Locate every Plasmodium falciparum-infected red blood cell.
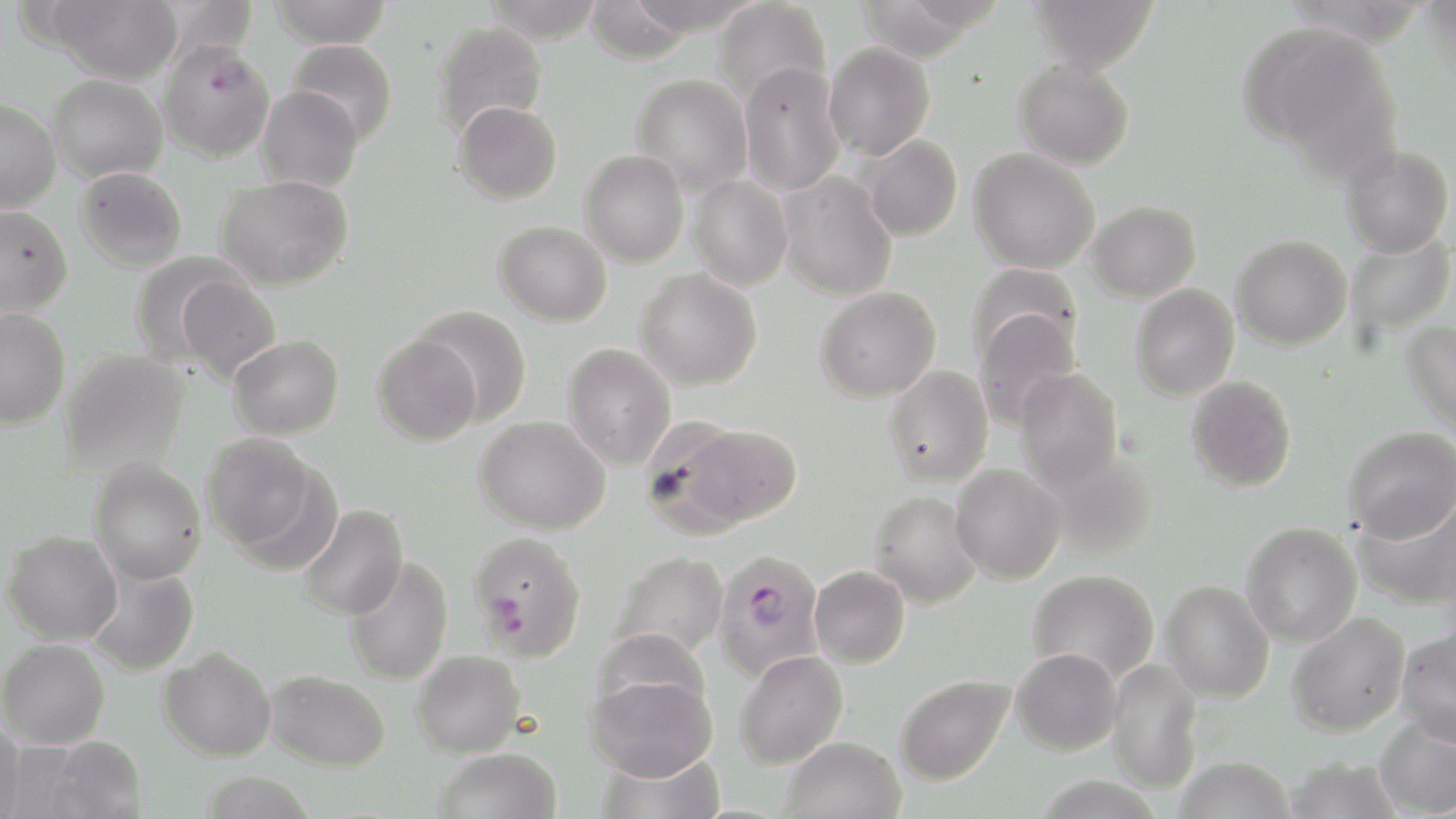
Approximate bounding boxes as [x1, y1, x2, y2] in pixels.
Plasmodium falciparum-infected red blood cells: [157, 39, 276, 162], [467, 530, 587, 661], [713, 550, 826, 681].

Uninfected red blood cell locations: [41, 0, 184, 84], [269, 0, 394, 49], [713, 0, 832, 109], [1027, 0, 1159, 72], [585, 1, 693, 64], [851, 1, 989, 62], [433, 20, 548, 137], [1238, 20, 1396, 162], [287, 39, 398, 146], [824, 41, 935, 160], [1014, 58, 1135, 169], [739, 62, 845, 197], [47, 73, 168, 183], [632, 73, 753, 197], [257, 85, 364, 193], [0, 98, 61, 212], [453, 100, 563, 204], [858, 134, 963, 242], [1340, 145, 1454, 258], [969, 148, 1100, 274], [579, 149, 689, 267], [75, 167, 187, 272], [777, 171, 898, 301], [216, 175, 353, 291], [688, 176, 793, 291], [1086, 200, 1201, 302], [0, 205, 73, 316], [494, 220, 612, 326], [1344, 231, 1454, 337], [1231, 234, 1352, 350], [130, 253, 243, 367], [968, 263, 1083, 365], [635, 268, 763, 391], [176, 275, 281, 384], [1130, 283, 1239, 400], [814, 286, 940, 403], [413, 305, 533, 426], [0, 307, 71, 429], [973, 310, 1083, 431], [1402, 319, 1456, 439], [372, 333, 482, 445], [228, 335, 344, 440], [562, 342, 677, 470], [60, 350, 189, 477], [883, 365, 993, 488], [1014, 368, 1124, 491], [1185, 374, 1297, 492], [474, 415, 610, 535], [670, 422, 802, 531], [1343, 426, 1456, 541], [201, 432, 321, 555], [89, 459, 207, 585], [950, 462, 1067, 584], [1352, 488, 1456, 610], [868, 490, 984, 609], [297, 504, 408, 621], [1241, 521, 1362, 648], [2, 530, 122, 645], [610, 551, 728, 661], [342, 556, 454, 686], [810, 565, 910, 668], [86, 566, 200, 677], [1027, 568, 1160, 684], [1159, 580, 1275, 703], [1286, 612, 1411, 736], [1395, 627, 1456, 745], [1, 638, 110, 748], [158, 646, 277, 762], [1011, 647, 1122, 755], [411, 650, 525, 758], [734, 650, 848, 768], [1106, 659, 1204, 793], [265, 669, 390, 771], [586, 672, 718, 781], [894, 673, 1015, 786], [1373, 714, 1456, 817], [0, 717, 25, 819], [38, 735, 149, 818], [780, 736, 906, 819], [433, 747, 562, 819], [595, 749, 725, 818], [1284, 753, 1404, 818], [1174, 755, 1296, 819], [199, 772, 315, 818], [1032, 774, 1166, 819]. Slide-level diagnosis: Plasmodium falciparum. 1000x magnification. Thin blood film. May-Grünwald-Giemsa-stained preparation. Image is 1456×819 pixels. One field of a larger specimen. Light microscopy.